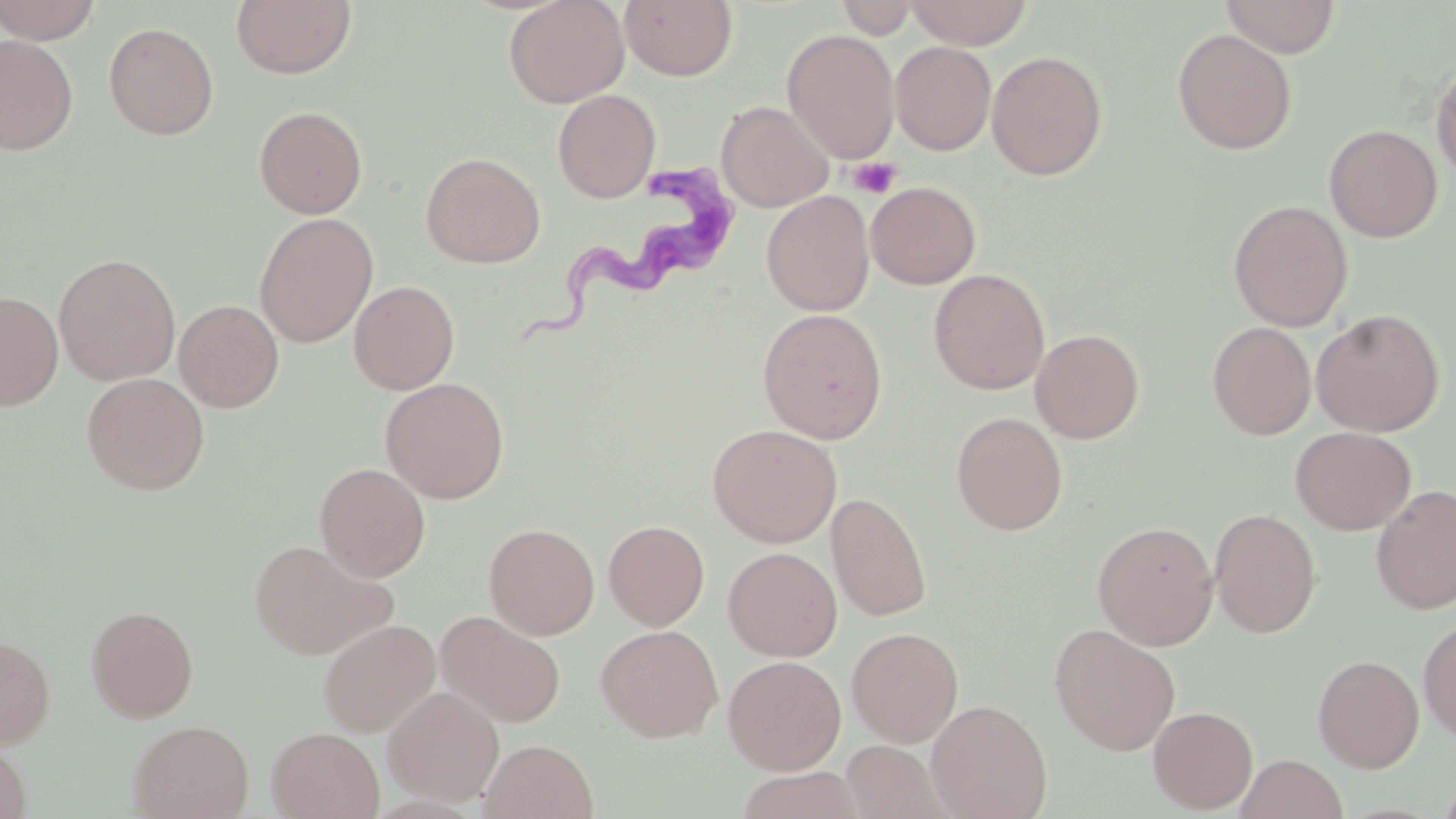
slide-level diagnosis = Trypanosoma brucei
magnification = 1000x
image size = 1456×819 pixels
stain = May-Grünwald-Giemsa
modality = light microscopy
preparation = thin blood smear
platelet locations = approximate bounding boxes as (x1, y1, x2, y2) in pixels: (848, 156, 901, 199)
uninfected red blood cell locations = approximate bounding boxes as (x1, y1, x2, y2) in pixels: (0, 0, 102, 44), (231, 0, 356, 79), (504, 0, 629, 108), (836, 0, 918, 39), (906, 0, 1033, 50), (1220, 0, 1341, 58), (620, 1, 738, 82), (103, 21, 219, 140), (782, 29, 900, 164), (1172, 29, 1297, 155), (0, 35, 79, 155), (890, 41, 997, 155), (987, 50, 1108, 180), (1431, 60, 1456, 183), (552, 89, 660, 203), (716, 101, 834, 212), (254, 105, 368, 219), (1324, 124, 1443, 242), (421, 151, 545, 268), (865, 181, 980, 289), (761, 191, 874, 316), (1228, 200, 1353, 331), (254, 212, 378, 347), (54, 253, 180, 385), (929, 269, 1050, 395), (349, 279, 460, 395), (0, 291, 63, 411), (174, 299, 284, 412), (757, 308, 888, 443), (1310, 308, 1445, 437), (1207, 321, 1316, 439), (1030, 328, 1145, 443), (81, 372, 210, 495), (380, 377, 509, 503), (951, 411, 1068, 535), (707, 424, 842, 547), (1290, 426, 1416, 535), (314, 462, 430, 581), (1371, 485, 1456, 615), (826, 492, 932, 621), (1209, 508, 1322, 638), (603, 520, 709, 630), (1092, 521, 1219, 650), (484, 523, 600, 639), (248, 538, 398, 660), (723, 546, 842, 661), (86, 604, 199, 722), (436, 610, 567, 728), (1418, 617, 1456, 742), (318, 619, 440, 737), (1049, 623, 1181, 755), (596, 624, 723, 742), (846, 626, 964, 747), (0, 633, 56, 748), (1312, 654, 1425, 773), (723, 655, 846, 774), (383, 686, 504, 806), (926, 699, 1052, 819), (1148, 705, 1258, 813), (128, 719, 253, 819), (266, 727, 384, 818), (480, 739, 598, 819), (0, 741, 31, 819), (841, 741, 950, 818), (1235, 754, 1347, 819), (733, 767, 868, 819)
Trypanosoma brucei locations = approximate bounding boxes as (x1, y1, x2, y2) in pixels: (521, 163, 737, 342)
field of view = single